State the preparation type.
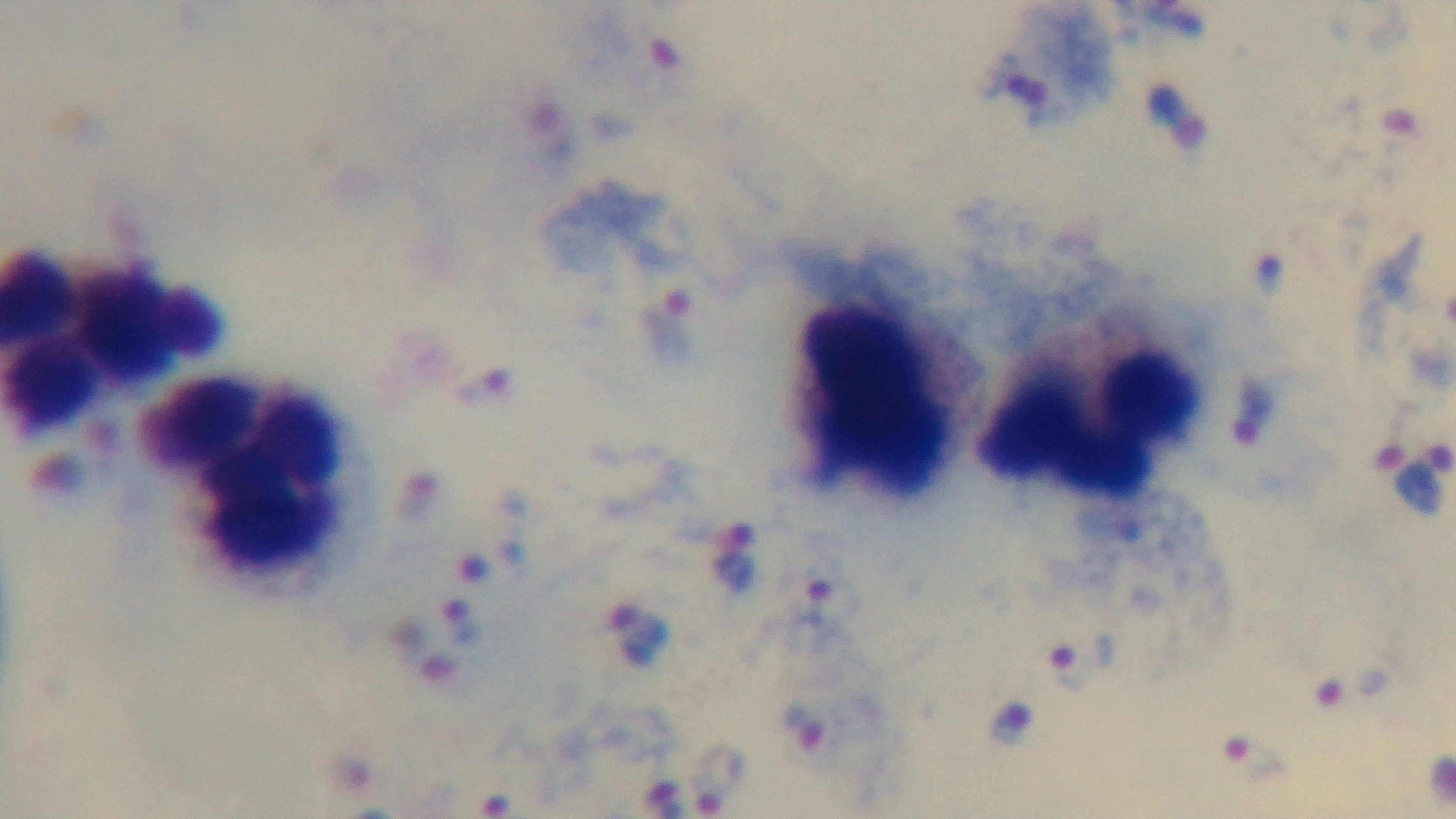

Thick.

Giemsa stain. Photomicrograph. Mounted 4K digital camera. Malaria status: infected. 100x oil-immersion objective. Single field of view.